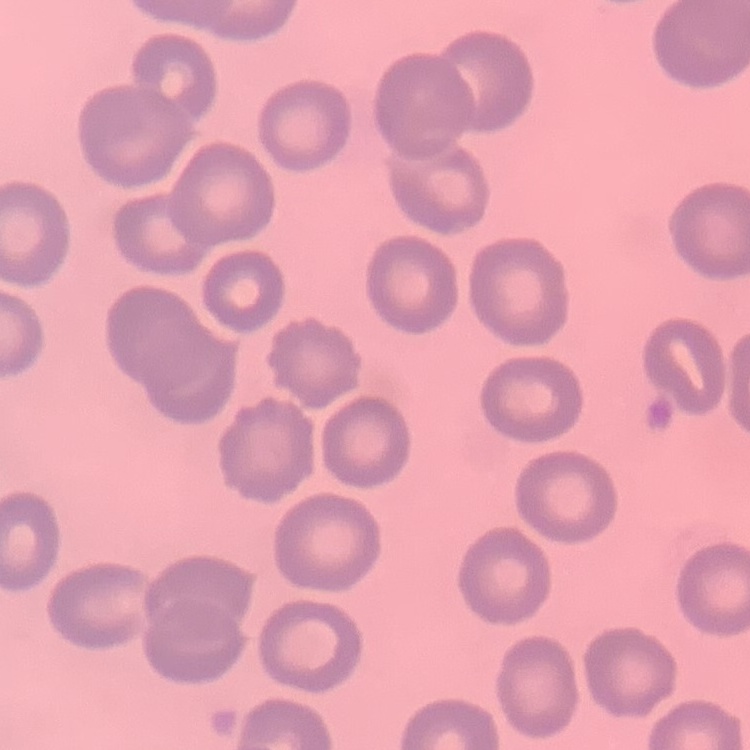

The red blood cells exhibit no rouleaux formation. Thin blood film. Square crop of a larger photomicrograph. Field's or Giemsa stain.